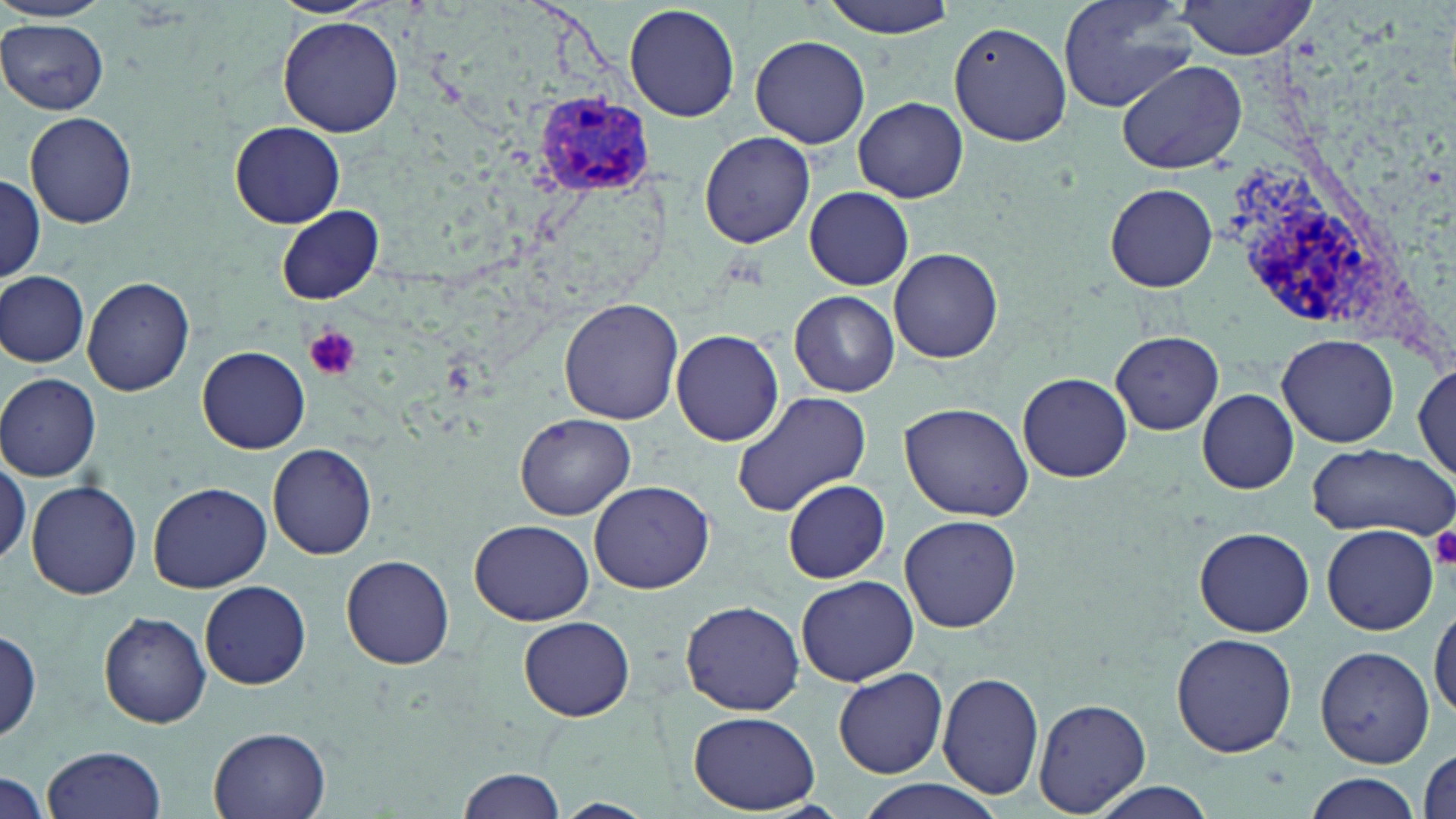 Approximate bounding boxes as [x1, y1, x2, y2] in pixels. Uninfected red blood cell locations: [815, 0, 960, 38], [1058, 0, 1196, 112], [1172, 1, 1321, 59], [625, 3, 740, 122], [278, 16, 404, 136], [0, 19, 109, 115], [950, 22, 1071, 147], [750, 34, 871, 149], [1118, 60, 1246, 173], [854, 97, 967, 203], [25, 110, 138, 229], [231, 122, 345, 228], [698, 131, 814, 248], [1, 175, 45, 285], [1106, 183, 1218, 292], [805, 186, 914, 291], [277, 205, 383, 304], [888, 247, 1003, 363], [1, 271, 90, 367], [82, 276, 194, 397], [789, 290, 900, 398], [559, 298, 685, 425], [671, 328, 785, 446], [1109, 331, 1225, 434], [1279, 335, 1398, 448], [199, 346, 309, 453], [1414, 362, 1454, 483], [1018, 372, 1132, 482], [0, 373, 101, 481], [1197, 388, 1299, 493], [730, 391, 873, 517], [901, 402, 1032, 521], [516, 413, 635, 520], [268, 443, 376, 560], [1305, 443, 1455, 538], [0, 457, 29, 567], [784, 478, 891, 584], [589, 480, 715, 594], [26, 481, 142, 601], [148, 482, 274, 593], [900, 515, 1021, 633], [471, 519, 594, 625], [1322, 525, 1437, 635], [1195, 526, 1314, 637], [342, 555, 455, 671], [796, 575, 918, 686], [199, 580, 311, 689], [1429, 599, 1456, 725], [680, 600, 804, 716], [97, 611, 212, 728], [519, 617, 635, 722], [1, 628, 44, 743], [1170, 633, 1298, 758], [1314, 646, 1433, 767], [835, 668, 948, 778], [937, 671, 1045, 800], [1034, 696, 1150, 816], [690, 711, 819, 813], [208, 726, 332, 819], [44, 744, 167, 819], [459, 767, 567, 819], [0, 770, 47, 818], [1300, 773, 1423, 819], [854, 780, 1004, 819], [1088, 784, 1219, 819], [552, 799, 657, 819]. Plasmodium vivax-infected red blood cell locations: [538, 94, 651, 196], [1216, 159, 1382, 348]. Platelet locations: [303, 326, 361, 381], [1429, 524, 1456, 569]. Slide-level diagnosis: Plasmodium vivax. Thin blood film. Light microscopy. Image is 1456×819 pixels. One field of a larger specimen. Captured at 1000x magnification. May-Grünwald-Giemsa-stained preparation.